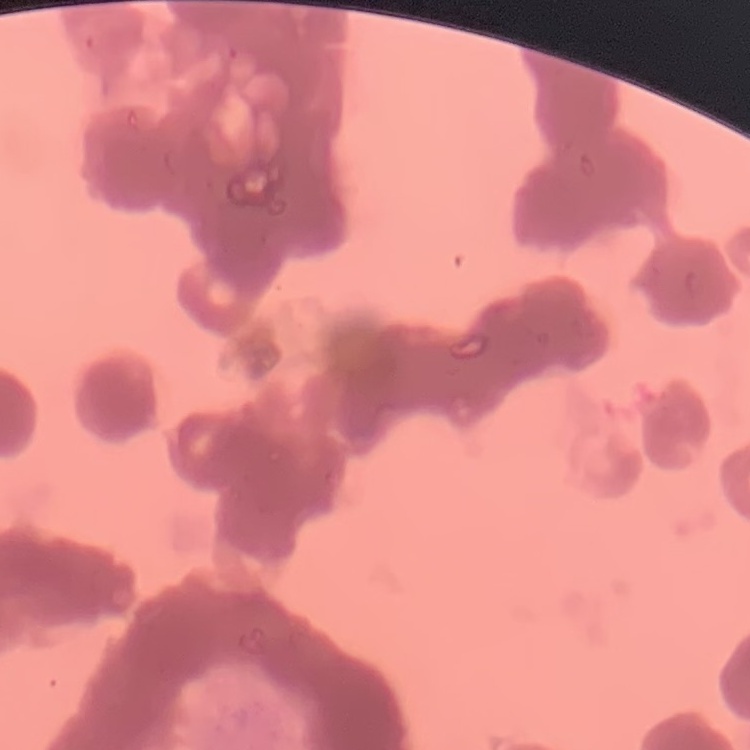
Summary:
  - Erythrocyte morphology: rouleaux formation
  - Stain: Field's or Giemsa
  - Image type: one tile cut from a larger photomicrograph
  - Preparation: thin blood film